Identify the blood parasite species.
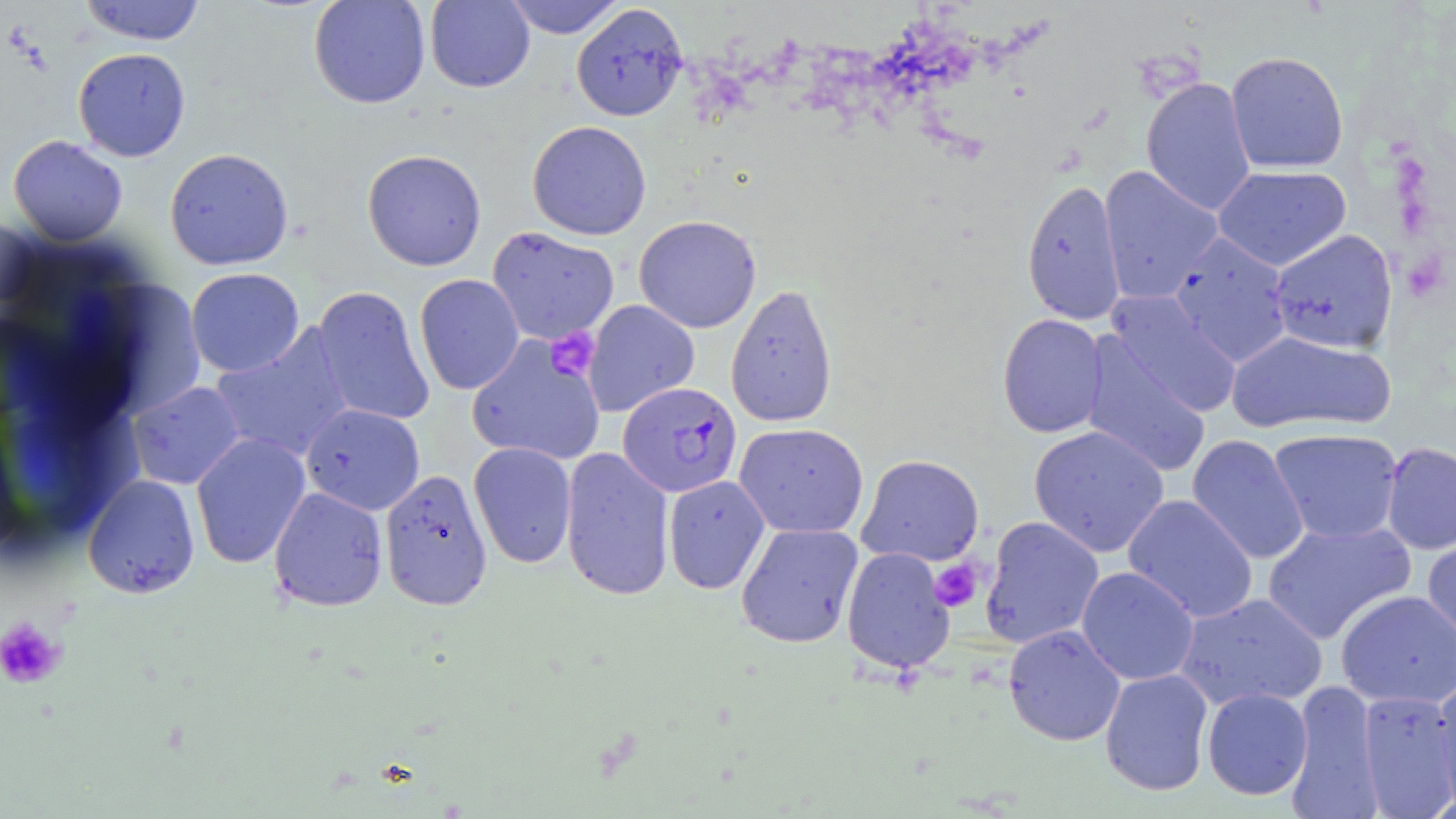

Plasmodium falciparum.

preparation = thin blood smear
magnification = 1000x
Plasmodium falciparum-infected red blood cell locations = approximate bounding boxes as named x1/y1/x2/y2 corners in pixels: (x1=618, y1=381, x2=742, y2=498)
modality = light microscopy
platelet locations = approximate bounding boxes as named x1/y1/x2/y2 corners in pixels: (x1=545, y1=328, x2=599, y2=380), (x1=930, y1=560, x2=984, y2=612), (x1=0, y1=615, x2=66, y2=689)
image size = 1456×819 pixels
stain = May-Grünwald-Giemsa
uninfected red blood cell locations = approximate bounding boxes as named x1/y1/x2/y2 corners in pixels: (x1=79, y1=0, x2=206, y2=45), (x1=308, y1=0, x2=430, y2=109), (x1=424, y1=0, x2=535, y2=92), (x1=503, y1=0, x2=625, y2=38), (x1=571, y1=3, x2=688, y2=121), (x1=73, y1=47, x2=191, y2=162), (x1=1225, y1=51, x2=1349, y2=173), (x1=1141, y1=77, x2=1257, y2=216), (x1=527, y1=120, x2=651, y2=240), (x1=8, y1=135, x2=128, y2=245), (x1=164, y1=148, x2=294, y2=270), (x1=362, y1=149, x2=487, y2=271), (x1=1098, y1=165, x2=1223, y2=304), (x1=1213, y1=165, x2=1351, y2=271), (x1=1021, y1=177, x2=1126, y2=326), (x1=634, y1=214, x2=761, y2=333), (x1=487, y1=226, x2=620, y2=345), (x1=1268, y1=228, x2=1399, y2=355), (x1=1169, y1=233, x2=1293, y2=367), (x1=185, y1=267, x2=304, y2=377), (x1=414, y1=274, x2=525, y2=395), (x1=725, y1=283, x2=838, y2=427), (x1=313, y1=286, x2=434, y2=426), (x1=1107, y1=291, x2=1242, y2=418), (x1=583, y1=300, x2=699, y2=416), (x1=997, y1=313, x2=1108, y2=438), (x1=210, y1=326, x2=354, y2=463), (x1=1226, y1=329, x2=1397, y2=436), (x1=1079, y1=333, x2=1212, y2=478), (x1=466, y1=336, x2=606, y2=465), (x1=127, y1=381, x2=245, y2=490), (x1=301, y1=403, x2=425, y2=515), (x1=734, y1=423, x2=869, y2=538), (x1=1029, y1=425, x2=1169, y2=557), (x1=1268, y1=428, x2=1403, y2=544), (x1=191, y1=433, x2=310, y2=569), (x1=1187, y1=434, x2=1309, y2=565), (x1=468, y1=441, x2=577, y2=569), (x1=1380, y1=442, x2=1456, y2=555), (x1=560, y1=446, x2=675, y2=602), (x1=856, y1=454, x2=984, y2=566), (x1=379, y1=468, x2=492, y2=611), (x1=83, y1=475, x2=200, y2=598), (x1=663, y1=475, x2=770, y2=594), (x1=268, y1=486, x2=388, y2=612), (x1=1123, y1=495, x2=1259, y2=623), (x1=979, y1=516, x2=1104, y2=649), (x1=1262, y1=519, x2=1416, y2=644), (x1=735, y1=522, x2=864, y2=649), (x1=1422, y1=530, x2=1456, y2=655), (x1=841, y1=546, x2=956, y2=674), (x1=1076, y1=566, x2=1199, y2=686), (x1=1335, y1=590, x2=1456, y2=709), (x1=1175, y1=592, x2=1328, y2=712), (x1=1003, y1=625, x2=1126, y2=746), (x1=1099, y1=668, x2=1214, y2=796), (x1=1431, y1=674, x2=1456, y2=813), (x1=1287, y1=680, x2=1382, y2=818), (x1=1202, y1=687, x2=1313, y2=800), (x1=1357, y1=689, x2=1456, y2=816)
field of view = one of a larger specimen